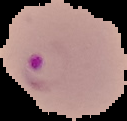

Summary:
  - Preparation: thin blood smear
  - Result: Plasmodium parasites detected
  - Image size: 127×121 pixels
  - Image type: segmented cell region on a black background